Describe the morphology of the erythrocytes.
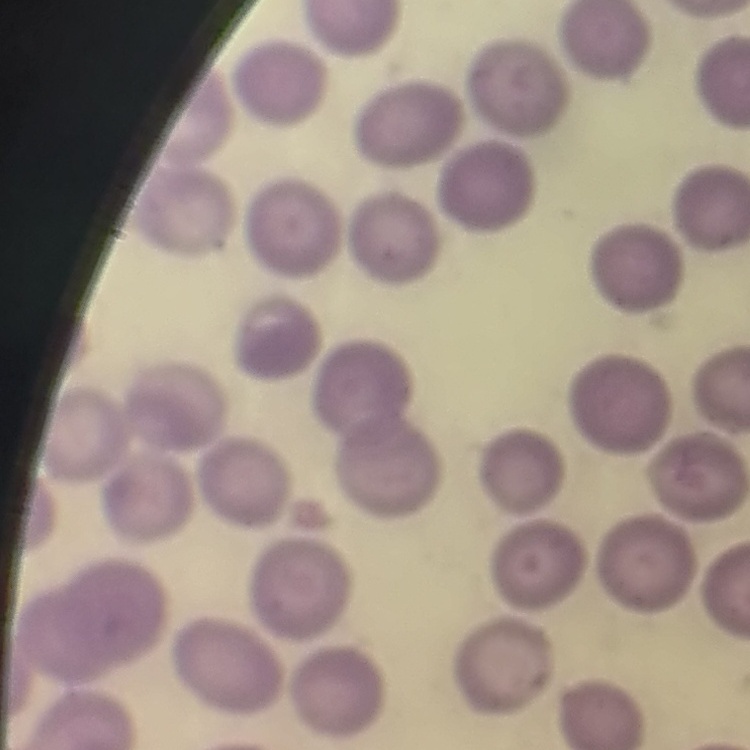
They show no rouleaux formation.

preparation: thin blood film
stain: Field's or Giemsa
image_type: one tile cut from a larger photomicrograph